Assess this cell for malaria.
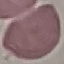

Uninfected.

Automatically extracted cell patch, resized to 64 × 64 pixels. Thin smear of blood. Giemsa stain. Photographed with a smartphone camera at the microscope eyepiece.